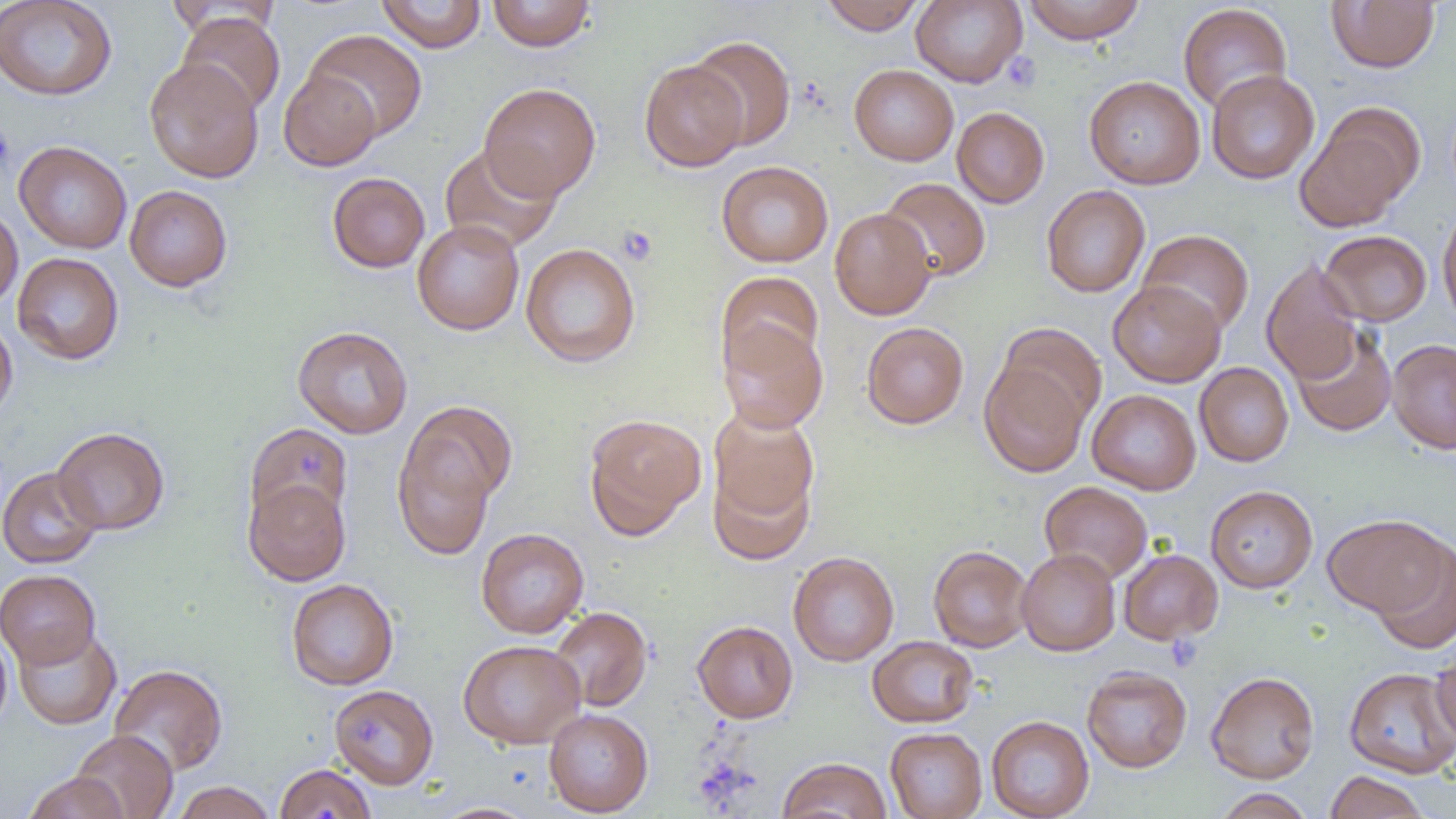

slide-level diagnosis = no evidence of blood parasites
magnification = 1000x
platelet locations = approximate bounding boxes as [x1, y1, x2, y2] in pixels: [1001, 52, 1041, 93], [0, 124, 16, 178], [617, 225, 659, 266], [1165, 633, 1203, 671]
image size = 1456×819 pixels
field of view = single
uninfected red blood cell locations = approximate bounding boxes as [x1, y1, x2, y2] in pixels: [0, 0, 117, 101], [376, 0, 487, 53], [487, 0, 597, 52], [820, 0, 926, 35], [911, 0, 1027, 87], [1022, 0, 1147, 44], [1326, 0, 1440, 73], [163, 1, 281, 41], [1177, 3, 1292, 113], [176, 11, 286, 116], [305, 29, 427, 141], [688, 35, 796, 151], [144, 58, 264, 183], [639, 60, 747, 171], [849, 64, 959, 166], [279, 69, 381, 171], [1206, 70, 1320, 184], [1084, 75, 1205, 189], [478, 82, 601, 200], [952, 107, 1050, 208], [1294, 110, 1419, 233], [14, 140, 132, 254], [438, 143, 562, 254], [716, 160, 834, 267], [327, 172, 430, 273], [879, 177, 991, 282], [124, 185, 232, 292], [1041, 185, 1150, 298], [1437, 203, 1456, 328], [0, 205, 23, 310], [829, 207, 936, 320], [412, 220, 525, 335], [1137, 229, 1254, 336], [1319, 229, 1432, 326], [520, 242, 640, 367], [12, 252, 124, 365], [1261, 259, 1365, 384], [716, 271, 824, 375], [1108, 280, 1226, 387], [0, 315, 18, 423], [718, 320, 829, 433], [861, 322, 969, 429], [997, 322, 1107, 430], [293, 325, 413, 439], [1290, 325, 1397, 436], [1387, 339, 1456, 453], [979, 359, 1090, 477], [1194, 362, 1294, 466], [1087, 389, 1201, 495], [404, 399, 516, 507], [708, 405, 820, 530], [583, 412, 707, 539], [245, 422, 353, 528], [53, 426, 169, 535], [392, 433, 497, 561], [708, 458, 815, 567], [0, 466, 103, 568], [243, 480, 350, 586], [1039, 481, 1153, 583], [1205, 485, 1318, 593], [1323, 514, 1450, 617], [476, 528, 589, 638], [1370, 540, 1456, 654], [928, 545, 1033, 652], [1016, 548, 1120, 656], [1118, 549, 1223, 645], [788, 551, 899, 666], [0, 569, 101, 669], [286, 578, 399, 690], [549, 606, 652, 712], [692, 620, 798, 723], [0, 626, 13, 735], [13, 626, 121, 730], [867, 636, 978, 728], [458, 639, 585, 749], [1431, 642, 1456, 748], [109, 664, 228, 776], [1082, 666, 1192, 773], [1344, 667, 1456, 778], [1206, 671, 1320, 783], [330, 684, 439, 789], [543, 708, 653, 817], [986, 715, 1095, 819], [885, 727, 987, 819], [71, 730, 179, 819], [777, 757, 891, 819], [274, 763, 376, 819], [1324, 770, 1430, 819], [22, 772, 129, 819], [172, 781, 278, 819], [1213, 789, 1315, 819], [430, 802, 542, 819]
preparation = thin blood film
modality = light microscopy